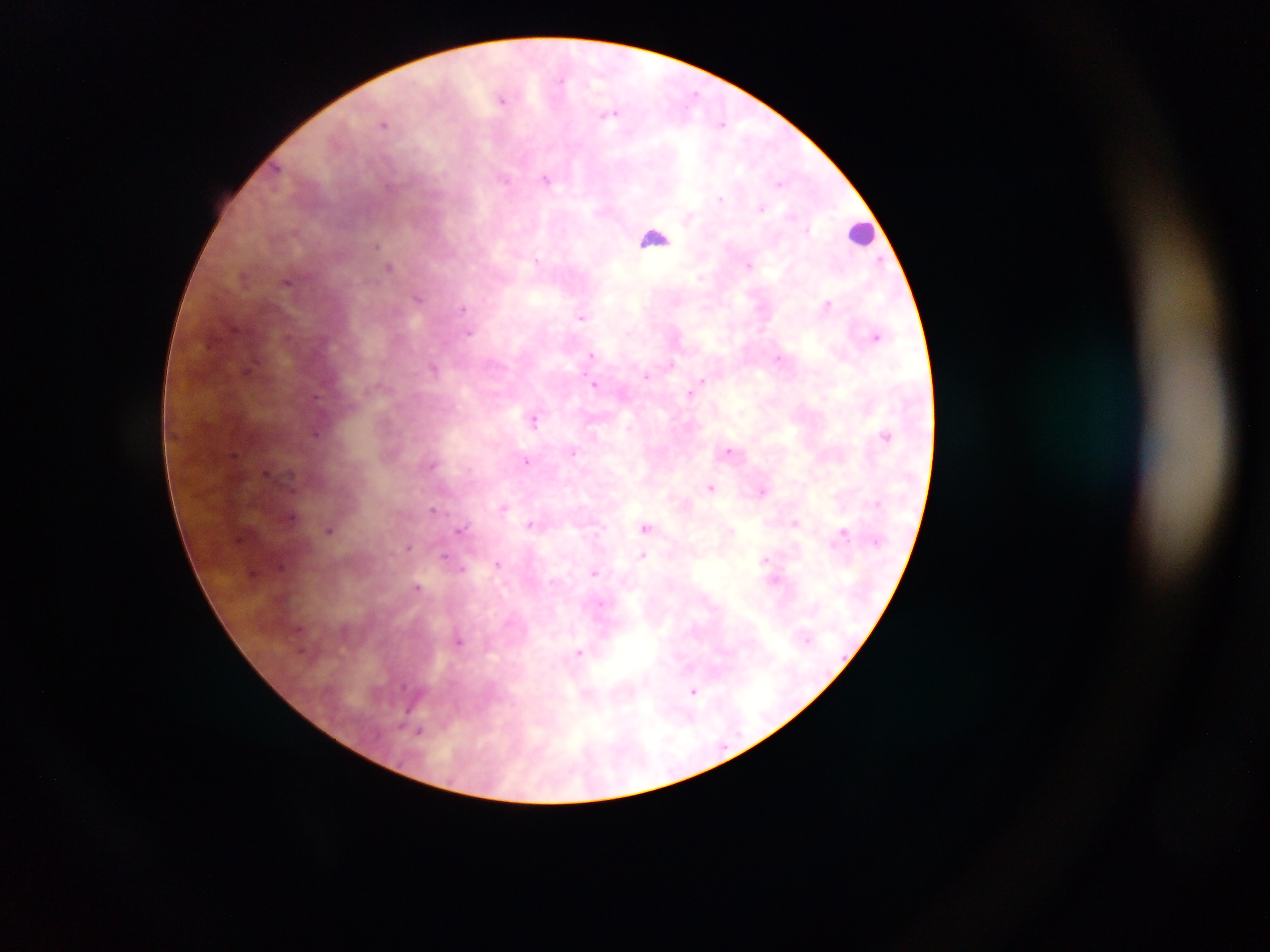

Approximate centers as [x, y] in pixels. Leukocyte locations: [862, 233], [653, 237]. Plasmodium parasite locations: [562, 80], [696, 93], [501, 99], [611, 114], [384, 124], [722, 124], [279, 167], [505, 179], [546, 179], [780, 184], [388, 186], [721, 198], [761, 207], [808, 229], [376, 246], [537, 260], [881, 260], [748, 265], [389, 267], [287, 282], [419, 299], [828, 304], [463, 308], [581, 317], [469, 333], [876, 337], [591, 354], [778, 358], [672, 363], [248, 369], [434, 369], [646, 376], [702, 380], [595, 384], [689, 395], [316, 398], [533, 420], [316, 434], [887, 436], [573, 451], [729, 451], [527, 461], [432, 464], [711, 487], [763, 490], [503, 507], [433, 509], [292, 516], [530, 523], [794, 523], [646, 527], [460, 528], [330, 530], [843, 533], [409, 546], [642, 555], [445, 556], [763, 560], [497, 564], [280, 566], [462, 569], [252, 573], [595, 573], [418, 587], [599, 605], [298, 629], [459, 640], [579, 652], [404, 687], [694, 691], [420, 731]. One field of view. Photographed through a microscope with a mobile-phone camera. Image is 1270×952 pixels. Sample from Ghana. Thick blood film.